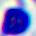

Micrograph. 400x magnification. A leukocyte is seen.